Outline each blood parasite and name the species.
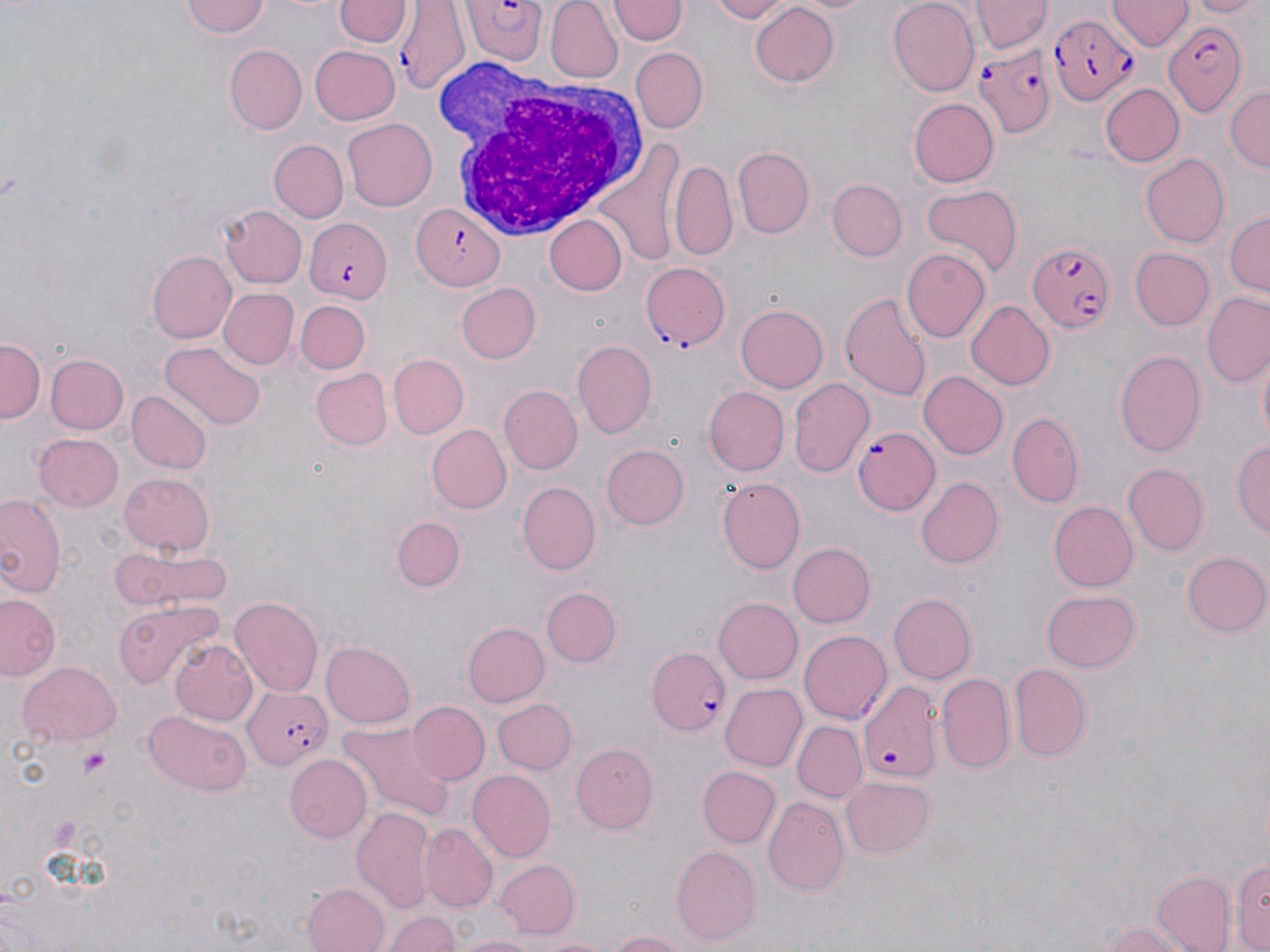

Approximate bounding boxes as (x1,y1)-(x2,y2) corner pairs in pixels.
Plasmodium falciparum-infected red blood cells: (462,2)-(544,66), (396,3)-(470,94), (1046,12)-(1135,107), (1161,18)-(1246,116), (971,41)-(1056,140), (411,201)-(508,291), (304,216)-(390,302), (1027,243)-(1114,332), (642,265)-(732,351), (854,425)-(939,516), (648,646)-(734,737), (857,678)-(942,784), (240,685)-(335,770).
No Plasmodium ovale, Plasmodium malariae, Plasmodium vivax, Babesia divergens, or Trypanosoma brucei observed.

Platelet locations: (80,746)-(111,779). White blood cell locations: (434,59)-(653,247). Uninfected red blood cell locations: (181,0)-(271,39), (334,0)-(410,49), (545,0)-(621,83), (612,0)-(683,46), (708,0)-(791,23), (787,0)-(878,15), (886,0)-(978,95), (1188,0)-(1262,18), (972,1)-(1049,56), (1107,1)-(1190,52), (749,4)-(840,88), (224,44)-(307,133), (311,45)-(399,124), (632,48)-(708,131), (1099,83)-(1184,167), (1225,83)-(1270,172), (909,98)-(998,186), (343,117)-(437,210), (590,138)-(684,271), (268,139)-(348,224), (733,146)-(814,237), (1138,153)-(1230,248), (669,157)-(737,261), (824,178)-(907,262), (920,183)-(1023,275), (220,204)-(307,289), (1225,211)-(1270,296), (545,216)-(625,297), (1130,247)-(1214,330), (901,248)-(990,344), (149,250)-(239,342), (455,283)-(543,364), (219,288)-(300,369), (839,292)-(934,402), (1201,294)-(1270,387), (965,299)-(1054,391), (297,302)-(369,373), (735,303)-(829,392), (0,336)-(45,421), (571,338)-(657,441), (162,343)-(264,430), (1117,349)-(1206,457), (44,352)-(129,436), (1255,352)-(1269,450), (389,354)-(468,438), (312,368)-(392,449), (919,372)-(1007,459), (787,377)-(875,478), (501,384)-(580,473), (704,387)-(788,474), (127,390)-(209,474), (1009,412)-(1084,506), (426,424)-(511,514), (33,432)-(124,512), (1232,436)-(1269,542), (599,443)-(689,530), (1121,464)-(1208,556), (118,472)-(217,555), (915,475)-(1004,568), (717,478)-(807,573), (519,483)-(601,576), (0,495)-(66,601), (1048,498)-(1138,592), (386,512)-(468,595), (787,543)-(875,629), (109,546)-(235,620), (108,549)-(173,609), (1182,551)-(1269,638), (542,586)-(621,667), (1042,590)-(1141,673), (1,593)-(62,682), (889,594)-(976,684), (230,595)-(324,698), (713,598)-(802,684), (113,603)-(223,690), (461,618)-(551,706), (799,630)-(893,724), (169,638)-(258,727), (321,641)-(415,727), (18,660)-(121,745), (1009,662)-(1091,763), (936,674)-(1016,777), (719,682)-(806,772), (491,698)-(576,773), (407,701)-(491,785), (146,710)-(251,794), (791,720)-(868,801), (341,722)-(459,823), (571,741)-(658,834), (282,753)-(371,843), (697,765)-(779,846), (469,770)-(555,860), (839,776)-(936,859), (762,796)-(848,898), (352,807)-(435,917), (421,823)-(496,910), (671,844)-(761,946), (491,856)-(580,939), (1229,856)-(1270,951), (1183,860)-(1270,952), (1152,873)-(1236,952), (304,882)-(392,952), (386,909)-(461,952), (1098,920)-(1191,952), (605,929)-(689,952), (534,931)-(612,952), (453,933)-(545,952). Slide-level diagnosis: Plasmodium falciparum. Image is 1270×952 pixels. May-Grünwald-Giemsa-stained preparation. Thin blood smear. One field of a larger specimen. 1000x magnification. Optical microscopy.